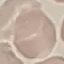
Malaria status: uninfected. Cell patch, automatically extracted from a larger field of view and resized to 64 × 64 pixels. Giemsa-stained preparation. Thin smear of blood. Photographed with a smartphone camera at the microscope eyepiece.